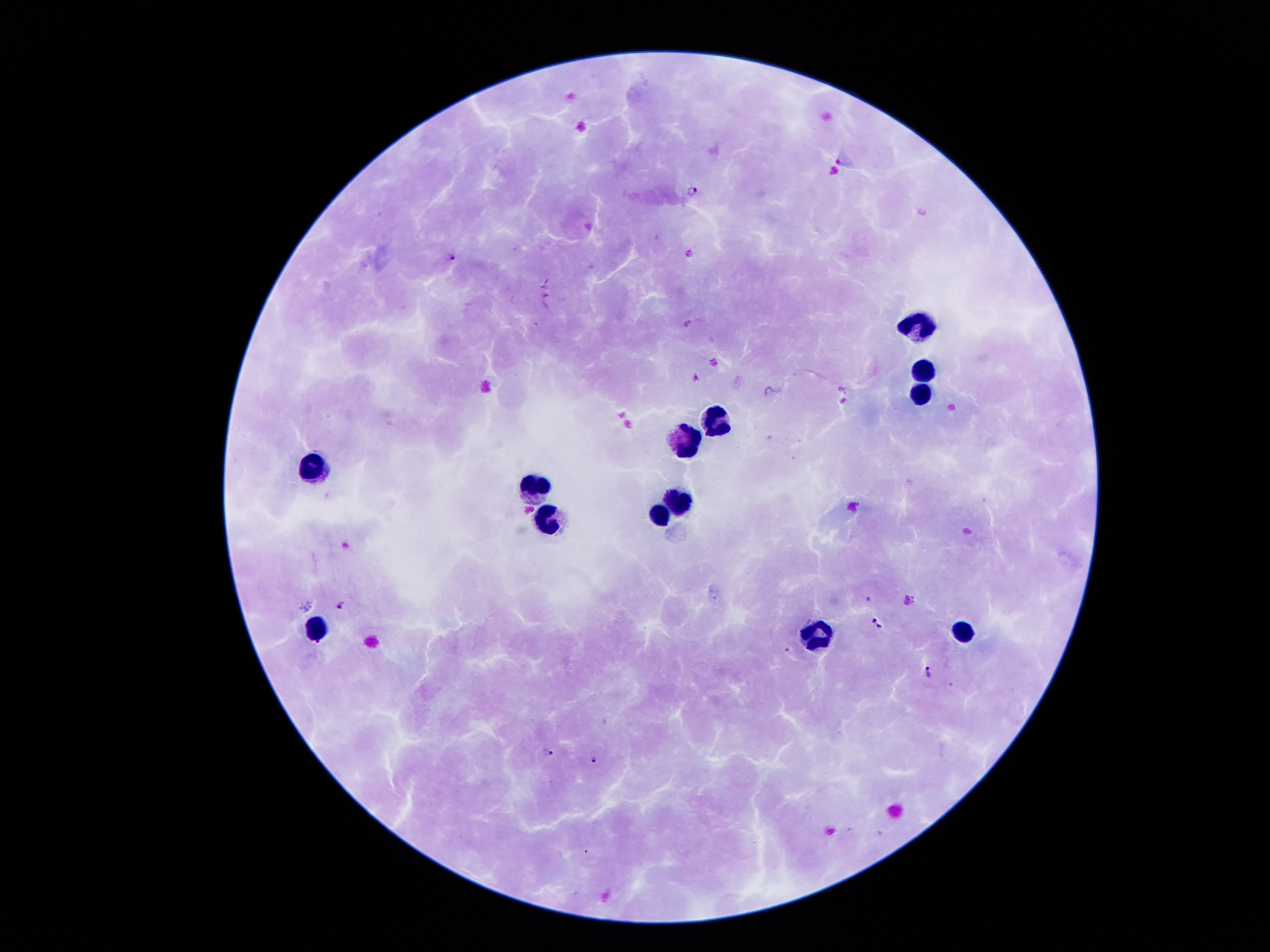
Approximate centers as (x, y) in pixels. Plasmodium parasite locations: (693, 190), (690, 253), (451, 257), (685, 322), (867, 598), (908, 600), (340, 605), (878, 623), (927, 672), (547, 752), (594, 759). Leukocyte locations: (915, 326), (926, 371), (920, 393), (715, 421), (688, 444), (317, 468), (532, 489), (680, 499), (660, 517), (549, 519), (315, 629), (962, 631), (814, 635). Patient malaria status: infected with Plasmodium falciparum. Thick blood film. Image is 1270×952 pixels. Giemsa-stained preparation. 100x magnification. One field from this slide. Smartphone photograph taken through the microscope eyepiece.